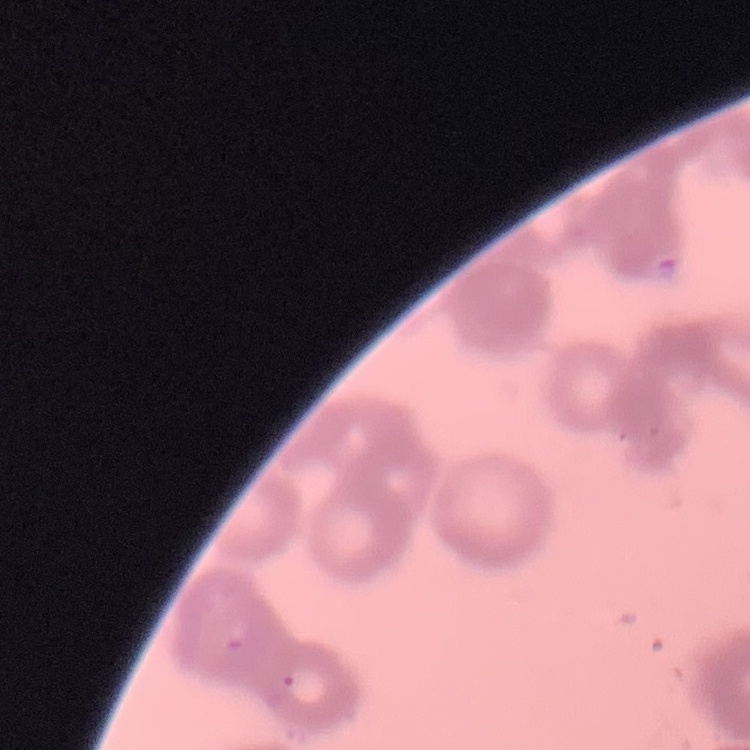

red blood cell morphology = rouleaux formation
preparation = thin blood film
stain = Field's or Giemsa
image type = square crop of a larger photomicrograph